Look for Plasmodium parasites.
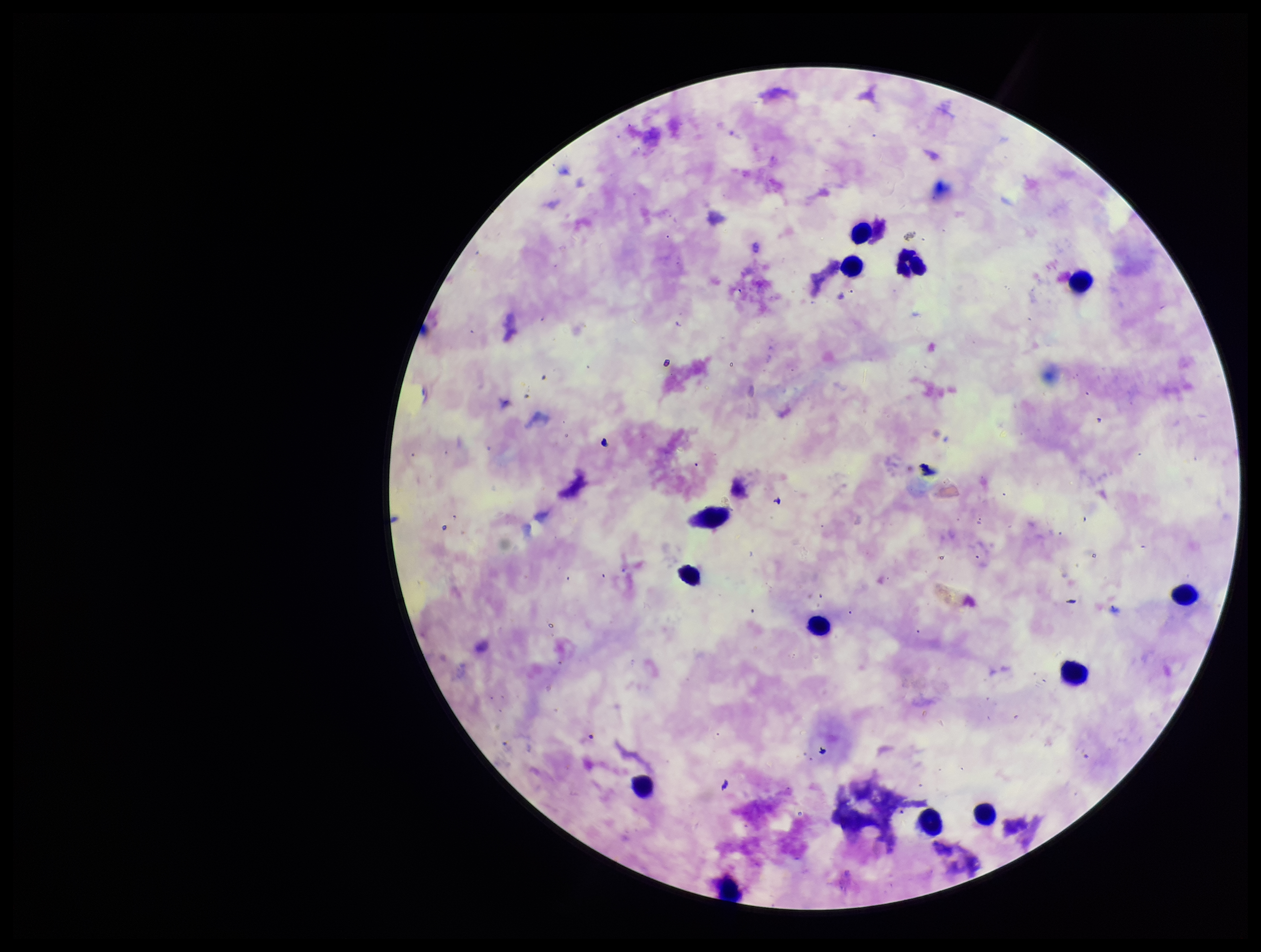
None detected.

Summary:
  - Stain: Giemsa
  - Image size: 1261×952 pixels
  - Parasite count: 0
  - Preparation: thick smear
  - Leukocyte count: 13
  - Capture: smartphone photograph through the microscope eyepiece
  - Field of view: one from this slide
  - Patient malaria status: infected
  - Species reported for this patient: Plasmodium falciparum